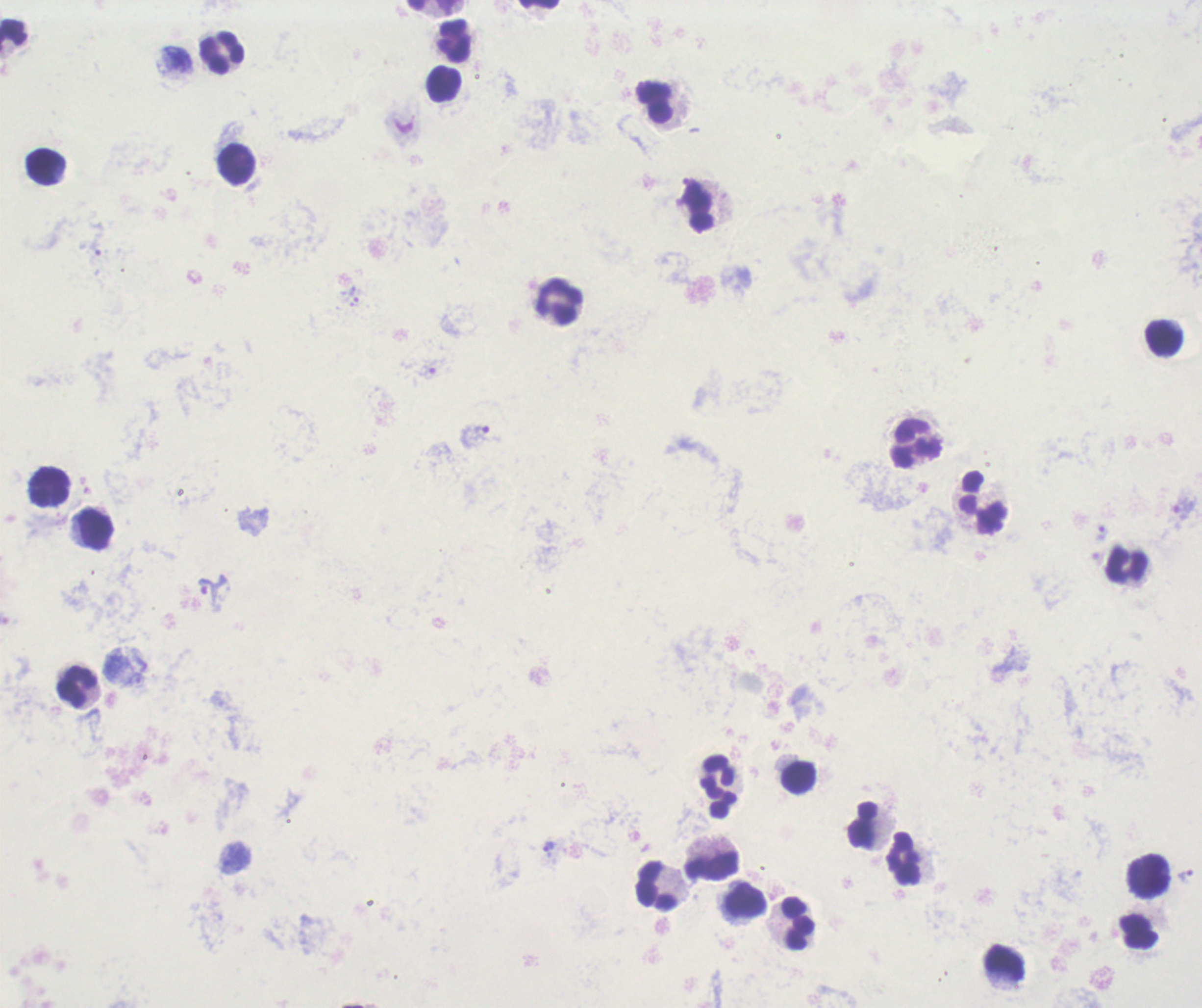

coordinate format = approximate centers as (x, y) in pixels
trophozoite locations = (475, 433), (1183, 506), (212, 589), (549, 847), (1187, 877)
leukocyte locations = (540, 4), (431, 5), (14, 35), (454, 41), (221, 54), (443, 85), (654, 103), (236, 166), (46, 168), (698, 208), (559, 302), (1165, 338), (915, 444), (47, 486), (983, 506), (94, 526), (1126, 567), (77, 688), (799, 777), (719, 785), (863, 824), (905, 860), (711, 868), (1149, 877), (657, 886), (747, 901), (795, 924), (1136, 933), (1006, 968)
preparation = thick smear of blood
background quality = unsatisfactory
stain = Romanowsky
magnification = 100x
field of view = single
result = malaria parasites identified
context = previously used in an actual diagnosis
image size = 1202×1008 pixels